Classify this cell by malaria status.
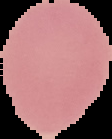

Uninfected.

Summary:
  - Image size: 112×139 pixels
  - Image type: segmented cell region on a black background
  - Preparation: thin blood smear